Classify this cell by malaria status.
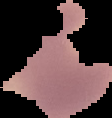

It is parasitized.

Cell region segmented out of the field of view; the surrounding area is masked to black. From a thin blood smear. Image is 112×118 pixels.